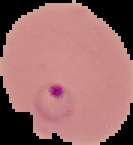

Summary:
  - Image size: 133×145 pixels
  - Malaria status: parasitized
  - Image type: segmented cell region with the area outside set to black
  - Preparation: thin blood film